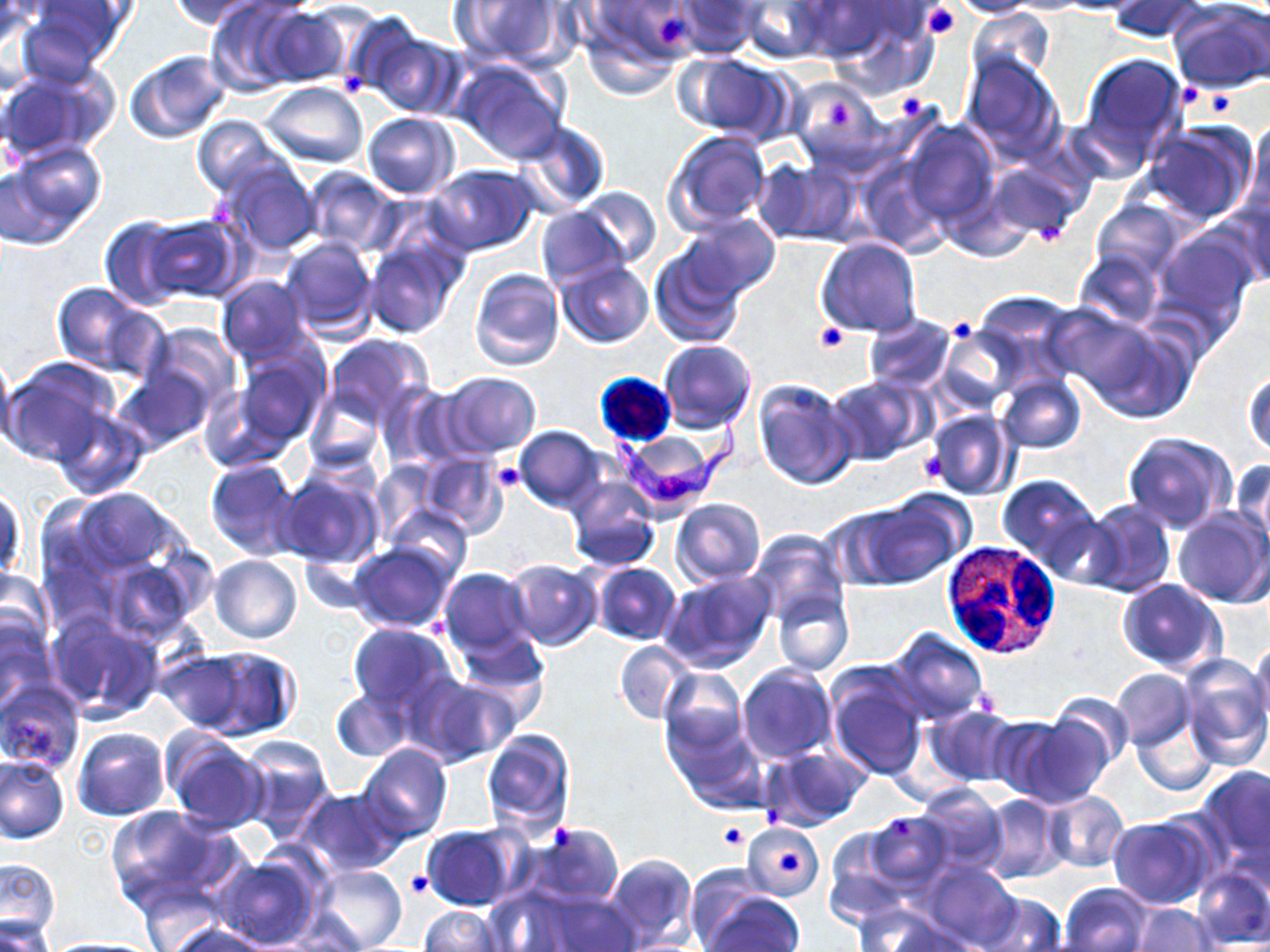
{
  "slide_level_diagnosis": "Trypanosoma brucei",
  "platelet_locations": "approximate bounding boxes as [x1, y1, x2, y2] in pixels: [922, 2, 962, 40], [656, 13, 688, 51], [338, 71, 369, 99], [1178, 83, 1199, 106], [1212, 93, 1233, 112], [899, 94, 925, 123], [831, 102, 851, 129], [1037, 221, 1061, 246], [953, 322, 971, 336], [814, 323, 846, 352], [918, 449, 946, 488], [490, 460, 528, 494], [765, 806, 783, 824], [889, 817, 911, 842], [718, 821, 749, 852], [547, 823, 574, 852], [779, 851, 802, 875], [403, 871, 433, 899]",
  "magnification": "1000x",
  "modality": "optical microscopy",
  "image_size": "1270×952 pixels",
  "white_blood_cell_locations": "approximate bounding boxes as [x1, y1, x2, y2] in pixels: [940, 538, 1063, 657]",
  "trypanosoma_brucei_locations": "approximate bounding boxes as [x1, y1, x2, y2] in pixels: [599, 407, 754, 510]",
  "stain": "May-Grünwald-Giemsa",
  "field_of_view": "single",
  "uninfected_red_blood_cell_locations": "approximate bounding boxes as [x1, y1, x2, y2] in pixels: [167, 0, 269, 30], [455, 0, 574, 70], [581, 0, 698, 89], [674, 0, 763, 58], [944, 0, 1049, 18], [1106, 0, 1208, 42], [739, 1, 832, 63], [203, 2, 305, 94], [0, 3, 39, 60], [20, 3, 132, 77], [921, 3, 961, 38], [1170, 3, 1270, 94], [256, 6, 353, 87], [821, 6, 936, 99], [966, 9, 1054, 87], [342, 12, 435, 106], [364, 28, 466, 119], [125, 49, 233, 143], [960, 51, 1067, 162], [676, 52, 795, 144], [1076, 52, 1191, 165], [453, 58, 568, 162], [0, 66, 111, 164], [785, 76, 886, 175], [260, 81, 369, 167], [362, 112, 459, 198], [191, 116, 288, 198], [1244, 116, 1270, 222], [900, 118, 998, 228], [518, 120, 611, 212], [1140, 122, 1260, 226], [667, 131, 771, 229], [2, 142, 106, 247], [856, 154, 950, 256], [984, 157, 1086, 243], [217, 160, 322, 255], [756, 160, 858, 246], [427, 164, 537, 255], [302, 167, 400, 255], [576, 186, 661, 269], [1225, 192, 1270, 290], [1091, 199, 1186, 279], [534, 206, 632, 291], [141, 213, 245, 303], [682, 214, 781, 300], [97, 216, 193, 309], [1150, 229, 1259, 344], [361, 235, 466, 338], [279, 236, 376, 341], [815, 237, 922, 339], [649, 246, 746, 349], [1075, 250, 1163, 328], [555, 259, 653, 347], [468, 267, 565, 373], [216, 275, 310, 363], [51, 283, 153, 375], [974, 292, 1082, 384], [1046, 303, 1162, 400], [863, 315, 955, 392], [1082, 317, 1199, 424], [142, 323, 241, 413], [935, 326, 1022, 413], [325, 335, 434, 428], [658, 339, 757, 433], [0, 348, 18, 451], [230, 349, 329, 450], [0, 357, 119, 467], [115, 363, 216, 453], [1244, 367, 1269, 459], [440, 371, 542, 455], [825, 375, 932, 466], [996, 375, 1087, 453], [752, 379, 858, 490], [382, 382, 467, 469], [304, 390, 383, 475], [50, 404, 150, 500], [925, 410, 1015, 500], [514, 425, 606, 512], [1123, 431, 1238, 534], [417, 452, 508, 536], [204, 457, 304, 561], [1231, 457, 1269, 553], [369, 460, 444, 542], [276, 468, 383, 569], [997, 473, 1101, 572], [564, 474, 660, 573], [1, 485, 25, 586], [44, 485, 201, 626], [671, 498, 766, 587], [850, 498, 963, 590], [1080, 499, 1175, 598], [384, 502, 471, 582], [1174, 508, 1270, 607], [747, 528, 848, 626], [346, 542, 456, 631], [294, 551, 380, 619], [210, 555, 303, 645], [505, 558, 601, 648], [590, 562, 681, 645], [437, 567, 537, 659], [0, 568, 56, 665], [661, 569, 776, 674], [1115, 579, 1225, 673], [837, 580, 933, 662], [773, 588, 854, 677], [47, 611, 165, 723], [0, 613, 53, 714], [347, 623, 459, 716], [884, 627, 991, 725], [455, 630, 549, 712], [1251, 639, 1270, 729], [613, 641, 695, 724], [166, 646, 299, 742], [1179, 655, 1269, 767], [736, 664, 837, 764], [659, 667, 748, 761], [1111, 668, 1194, 750], [826, 669, 928, 782], [413, 675, 520, 765], [0, 677, 85, 776], [330, 687, 412, 761], [1047, 692, 1136, 772], [925, 705, 1019, 787], [1132, 709, 1220, 797], [1015, 715, 1112, 809], [984, 716, 1076, 800], [666, 723, 766, 815], [73, 726, 170, 821], [481, 727, 575, 836], [237, 735, 334, 836], [162, 736, 266, 832], [358, 745, 453, 844], [762, 747, 870, 831], [0, 754, 69, 844], [1197, 765, 1270, 869], [912, 783, 1009, 873], [296, 787, 407, 876], [1042, 791, 1130, 873], [979, 794, 1069, 884], [105, 807, 242, 915], [862, 813, 955, 895], [1107, 815, 1215, 909], [743, 822, 824, 902], [524, 823, 623, 908], [422, 826, 521, 910], [604, 853, 697, 950], [210, 855, 321, 950], [0, 858, 60, 941], [921, 862, 1019, 948], [311, 864, 407, 951], [684, 864, 768, 945], [1190, 864, 1270, 949], [1059, 883, 1153, 952], [132, 889, 233, 952], [527, 891, 642, 950], [973, 892, 1067, 952], [703, 895, 805, 952], [852, 902, 954, 952], [1132, 903, 1218, 952], [418, 906, 504, 952], [0, 916, 53, 952], [166, 923, 268, 952], [38, 939, 165, 952]",
  "preparation": "thin blood film"
}